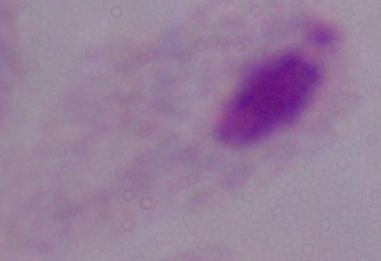
1000x magnification. A trichomonad is seen. Photomicrograph.